Name the parasite shown.
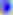

This is Toxoplasma gondii.

Summary:
  - Magnification: 400x
  - Modality: photomicrograph